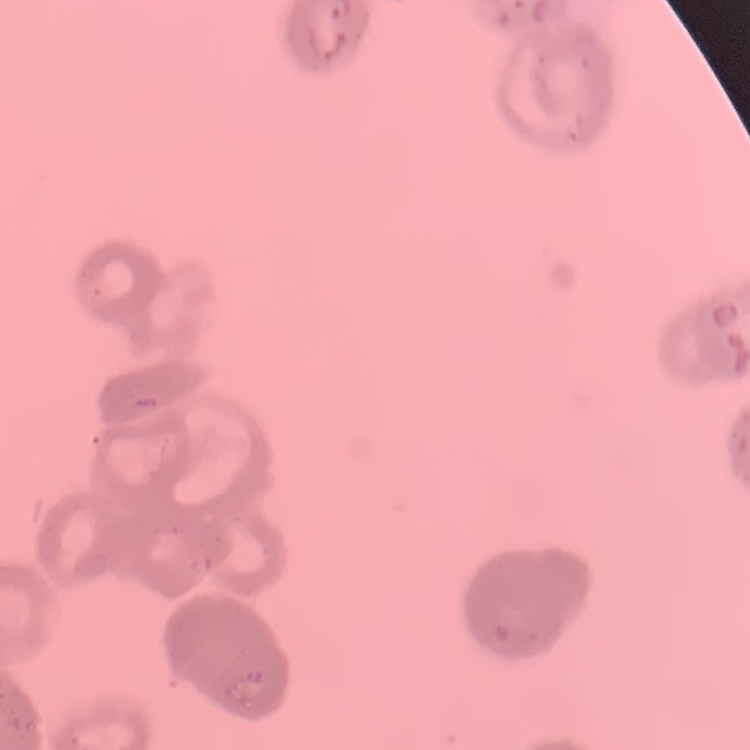

The erythrocytes exhibit rouleaux formation. Thin peripheral smear. One tile cut from a larger photomicrograph. Field's or Giemsa stain.